Report the malaria status of this cell.
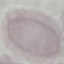
Uninfected.

{
  "image_type": "cell patch, automatically extracted from a larger field of view and resized to 64 × 64 pixels",
  "stain": "Giemsa",
  "capture": "smartphone through the microscope eyepiece",
  "preparation": "thin smear"
}